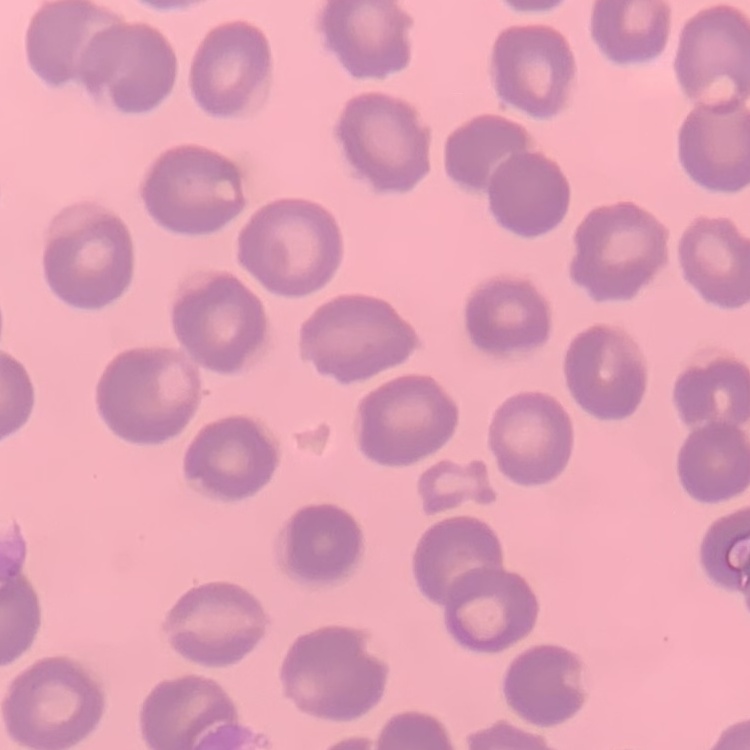
erythrocyte morphology = no rouleaux formation
preparation = thin blood smear
stain = Field's or Giemsa
image type = one tile cut from a larger photomicrograph